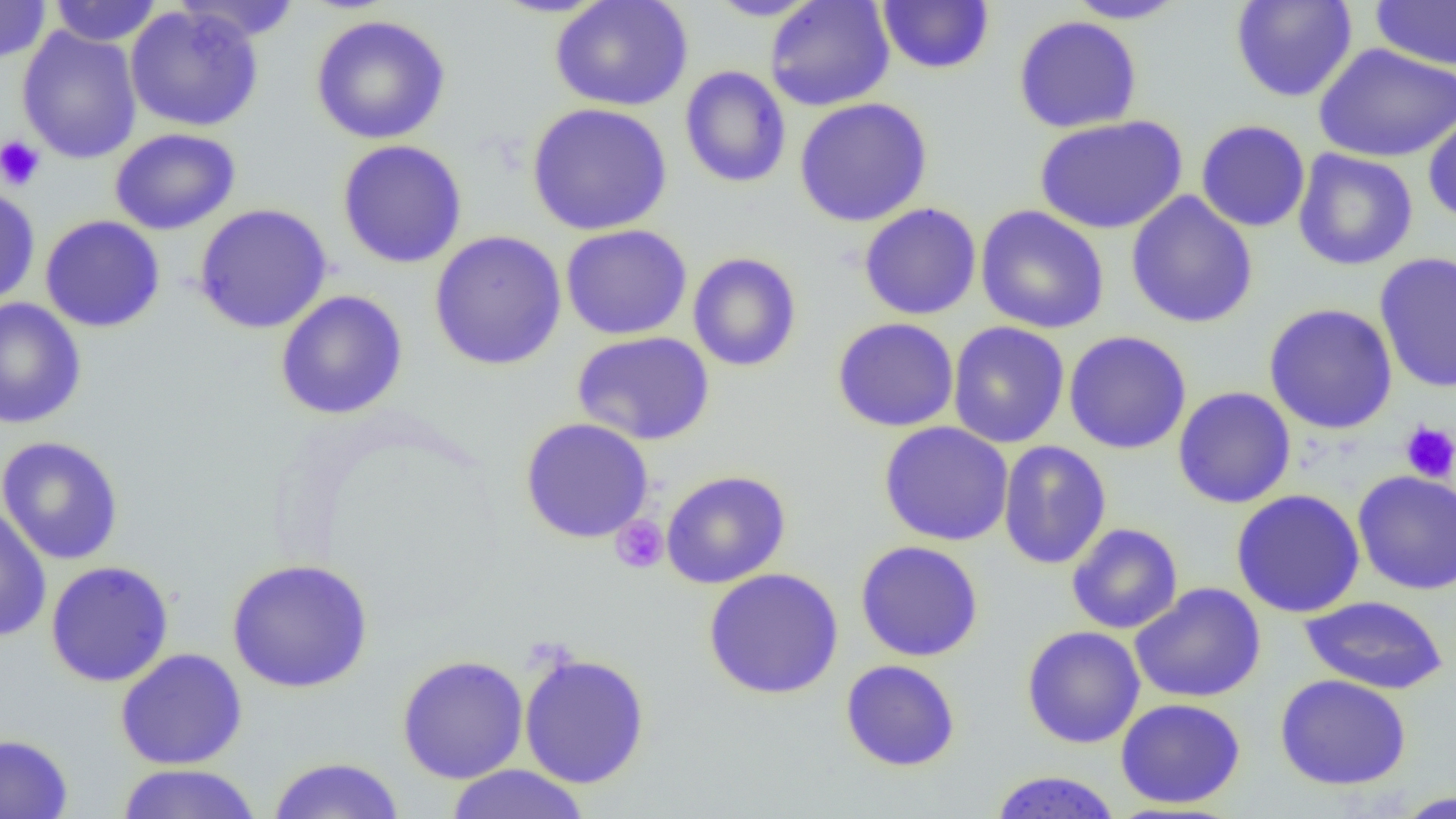

slide-level diagnosis = negative for blood parasites
preparation = thin blood smear
uninfected red blood cell locations = approximate bounding boxes as [x1, y1, x2, y2] in pixels: [48, 0, 163, 47], [172, 0, 302, 43], [704, 0, 823, 21], [764, 0, 895, 112], [877, 0, 994, 75], [1062, 0, 1192, 24], [1230, 0, 1358, 103], [0, 1, 51, 64], [550, 1, 693, 111], [1370, 1, 1456, 71], [125, 5, 264, 132], [310, 14, 451, 144], [1013, 15, 1143, 133], [16, 26, 142, 164], [1314, 43, 1456, 163], [679, 66, 792, 188], [794, 98, 933, 227], [526, 102, 673, 236], [1422, 111, 1456, 225], [1033, 115, 1188, 234], [1195, 119, 1310, 233], [109, 128, 241, 235], [337, 140, 468, 269], [1292, 148, 1418, 271], [0, 185, 40, 306], [1126, 191, 1258, 329], [858, 203, 982, 320], [193, 204, 332, 334], [975, 205, 1110, 334], [40, 215, 166, 333], [560, 224, 692, 340], [429, 230, 567, 371], [687, 251, 802, 372], [1373, 252, 1456, 394], [275, 290, 408, 420], [0, 298, 86, 430], [1263, 303, 1398, 434], [831, 317, 959, 432], [947, 321, 1070, 448], [1063, 330, 1192, 454], [572, 331, 715, 446], [1172, 386, 1296, 509], [520, 417, 654, 544], [878, 421, 1014, 546], [0, 435, 124, 565], [997, 440, 1112, 570], [1353, 469, 1456, 595], [660, 470, 792, 589], [1231, 489, 1366, 618], [0, 505, 52, 644], [1066, 522, 1183, 634], [855, 540, 984, 662], [226, 558, 374, 693], [45, 560, 174, 687], [703, 568, 843, 699], [1129, 582, 1266, 704], [1298, 595, 1449, 695], [1021, 625, 1145, 748], [115, 648, 248, 770], [518, 652, 651, 789], [396, 654, 529, 784], [840, 659, 961, 771], [1274, 674, 1412, 791], [1115, 697, 1246, 809], [0, 732, 73, 819], [267, 756, 407, 818], [114, 763, 264, 818], [443, 764, 592, 818], [988, 770, 1122, 819], [1391, 791, 1455, 818]
magnification = 1000x
field of view = single
platelet locations = approximate bounding boxes as [x1, y1, x2, y2] in pixels: [0, 135, 45, 191], [1399, 422, 1456, 484], [609, 515, 669, 574]
image size = 1456×819 pixels
modality = light microscopy